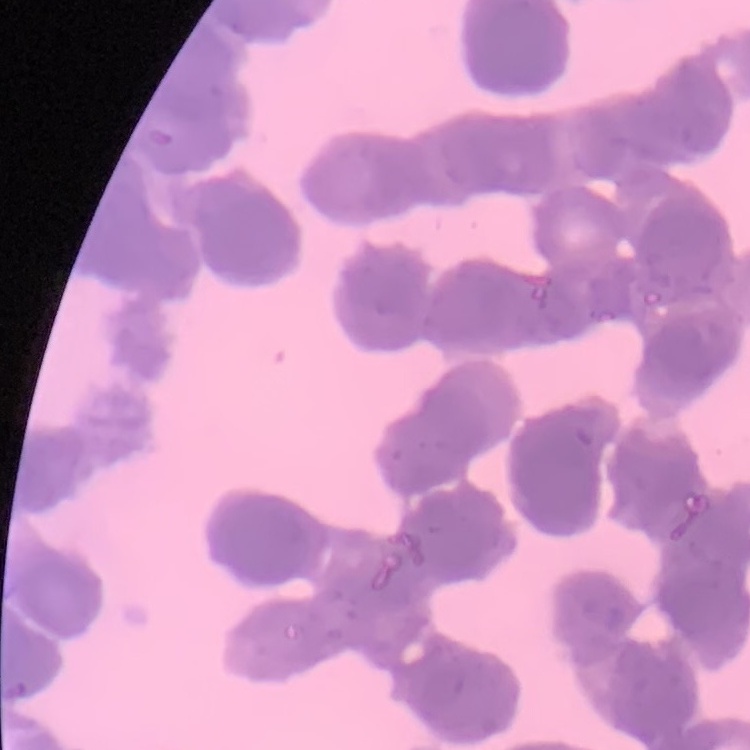
Summary:
  - Erythrocyte morphology: rouleaux formation
  - Preparation: thin peripheral smear
  - Image type: square crop of a larger photomicrograph
  - Stain: Field's or Giemsa